Report the malaria status of this cell.
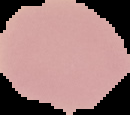

It is uninfected.

Summary:
  - Preparation: thin blood film
  - Image type: segmented cell region on a black background
  - Image size: 130×115 pixels